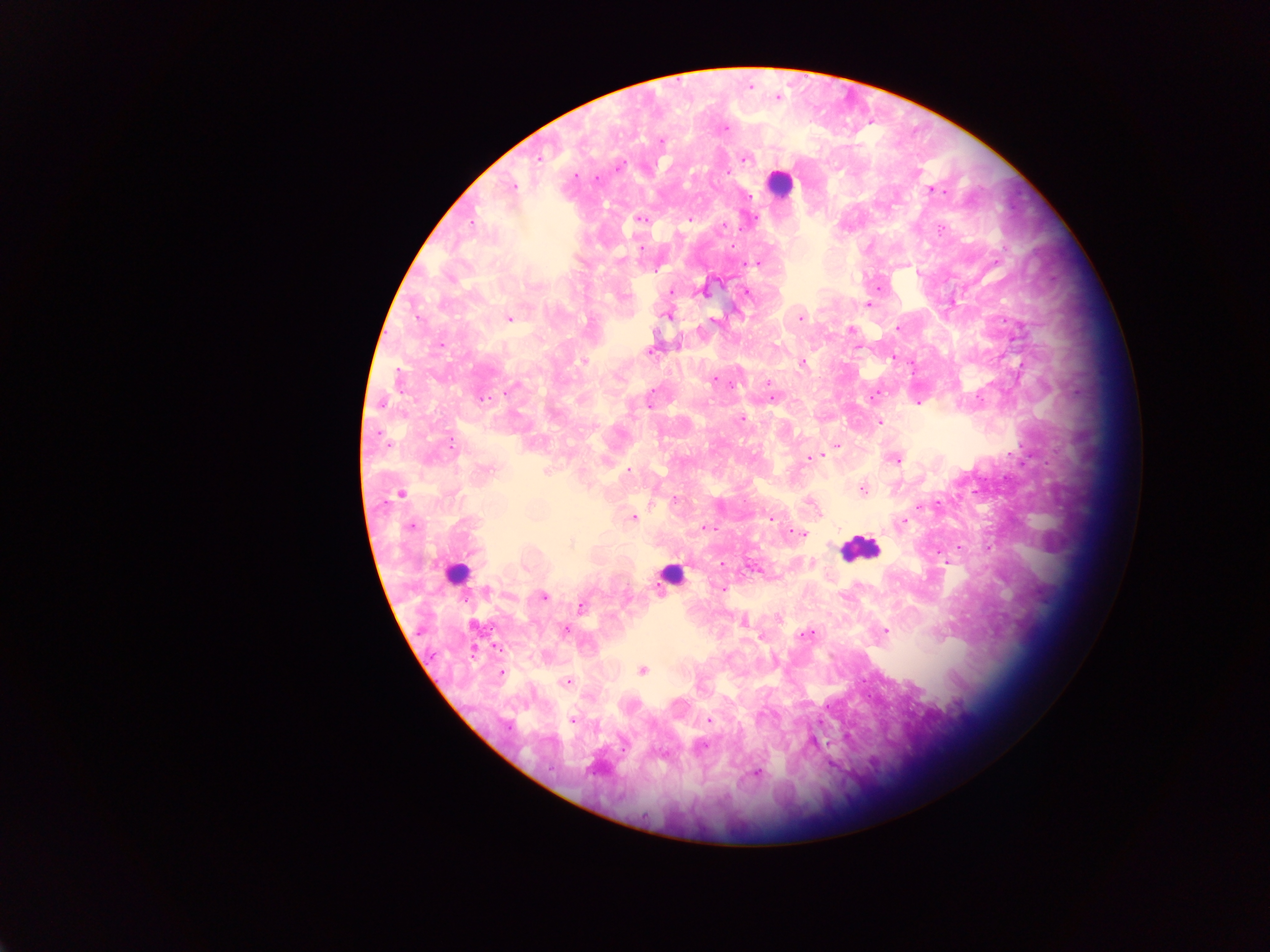
Approximate centers as x y in pixels.
Summary:
  - Malaria parasite locations: 750 87; 778 97; 725 128; 661 141; 538 158; 745 158; 728 172; 575 175; 597 179; 513 186; 933 190; 941 192; 751 196; 642 219; 690 219; 723 226; 941 230; 640 247; 621 261; 756 263; 671 292; 704 292; 746 292; 624 296; 868 304; 667 315; 800 318; 509 319; 713 320; 897 328; 851 330; 440 344; 650 350; 893 357; 584 362; 804 364; 715 380; 768 383; 733 386; 513 388; 653 390; 771 390; 872 397; 483 399; 775 399; 919 402; 381 404; 649 406; 742 418; 879 422; 451 442; 837 446; 809 458; 896 460; 487 468; 547 470; 629 470; 863 490; 400 493; 675 500; 745 501; 810 503; 919 507; 634 517; 771 518; 902 522; 412 527; 705 528; 801 533; 572 543; 958 548; 721 564; 724 588; 488 591; 543 596; 627 596; 581 607; 779 619; 743 621; 565 629; 886 631; 805 634; 762 638; 642 670; 501 673; 863 679; 567 681; 761 716; 572 720; 710 721; 623 745; 703 746; 758 773
  - Leukocyte locations: 780 184; 860 549; 455 574; 674 574
  - Preparation: thick blood smear
  - Field of view: single
  - Country: Ghana
  - Capture: mobile-phone photograph through a microscope
  - Image size: 1270×952 pixels